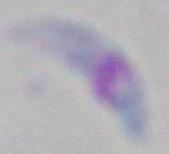

modality = micrograph
identification = Toxoplasma gondii
magnification = 1000x